Give the extent of all Plasmodium ovale-infected red blood cells.
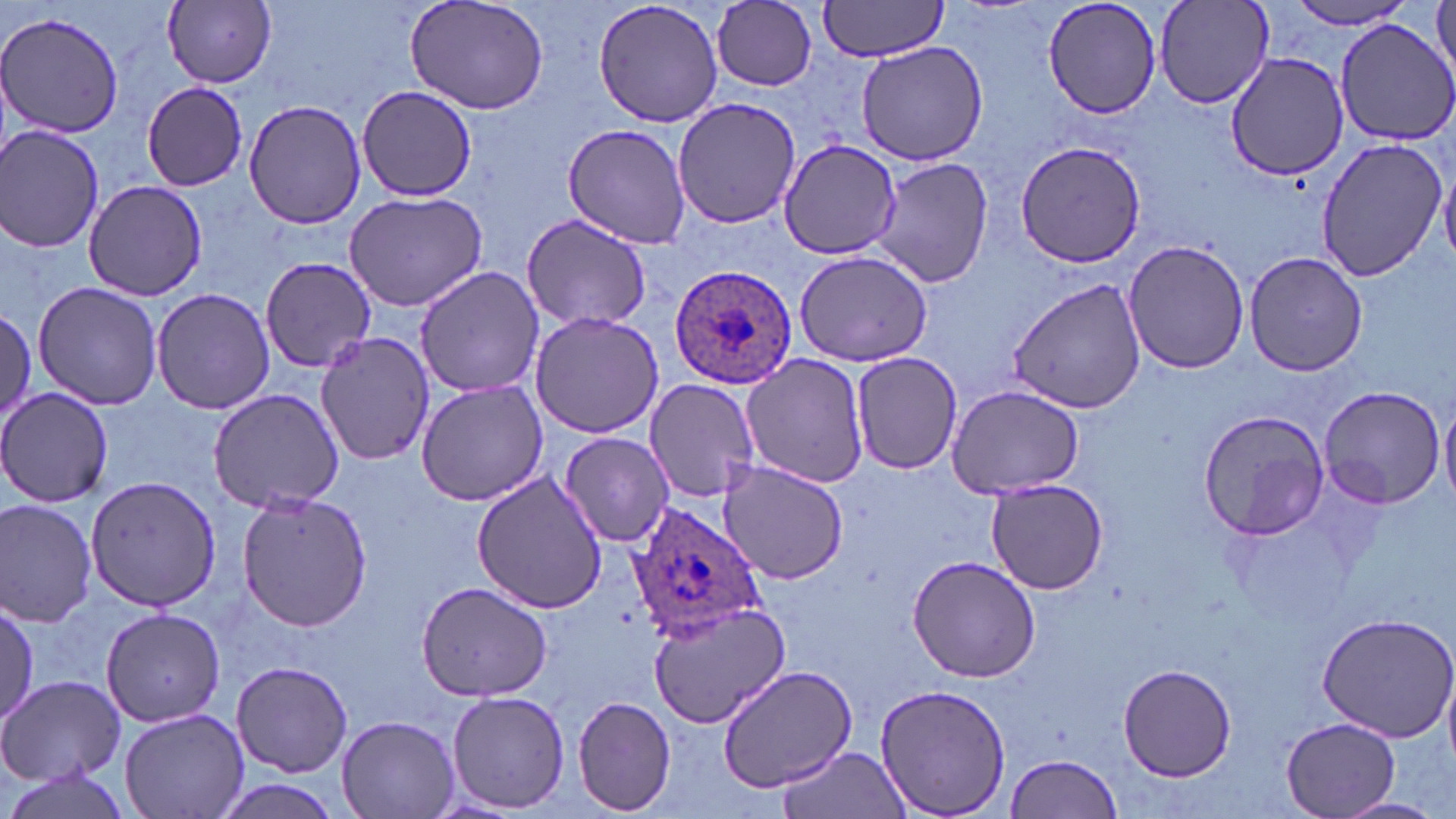

Approximate bounding boxes as named x1/y1/x2/y2 corners in pixels.
Plasmodium ovale-infected red blood cells: (x1=669, y1=262, x2=799, y2=389), (x1=626, y1=502, x2=766, y2=644).

slide-level diagnosis = Plasmodium ovale
modality = optical microscopy
image size = 1456×819 pixels
stain = May-Grünwald-Giemsa
magnification = 1000x
uninfected red blood cell locations = approximate bounding boxes as named x1/y1/x2/y2 corners in pixels: (x1=163, y1=0, x2=277, y2=88), (x1=404, y1=0, x2=552, y2=116), (x1=592, y1=0, x2=725, y2=129), (x1=817, y1=0, x2=953, y2=61), (x1=1043, y1=0, x2=1162, y2=120), (x1=1430, y1=0, x2=1456, y2=88), (x1=708, y1=1, x2=821, y2=93), (x1=1153, y1=2, x2=1274, y2=109), (x1=1282, y1=2, x2=1422, y2=30), (x1=1, y1=11, x2=125, y2=139), (x1=1332, y1=17, x2=1456, y2=147), (x1=854, y1=41, x2=990, y2=167), (x1=1224, y1=51, x2=1350, y2=182), (x1=142, y1=82, x2=249, y2=192), (x1=356, y1=85, x2=477, y2=202), (x1=672, y1=96, x2=804, y2=228), (x1=243, y1=98, x2=367, y2=230), (x1=561, y1=120, x2=694, y2=250), (x1=1, y1=125, x2=104, y2=253), (x1=1314, y1=134, x2=1447, y2=283), (x1=776, y1=138, x2=906, y2=260), (x1=1014, y1=140, x2=1145, y2=267), (x1=869, y1=156, x2=993, y2=290), (x1=1439, y1=162, x2=1456, y2=267), (x1=82, y1=179, x2=208, y2=300), (x1=343, y1=191, x2=487, y2=312), (x1=520, y1=213, x2=653, y2=334), (x1=1123, y1=239, x2=1251, y2=374), (x1=793, y1=249, x2=934, y2=368), (x1=1244, y1=250, x2=1366, y2=376), (x1=261, y1=259, x2=376, y2=374), (x1=414, y1=266, x2=547, y2=397), (x1=1007, y1=278, x2=1146, y2=413), (x1=32, y1=282, x2=164, y2=411), (x1=151, y1=286, x2=274, y2=415), (x1=0, y1=305, x2=35, y2=429), (x1=529, y1=311, x2=663, y2=439), (x1=316, y1=333, x2=437, y2=467), (x1=852, y1=352, x2=962, y2=475), (x1=741, y1=354, x2=872, y2=488), (x1=646, y1=377, x2=762, y2=501), (x1=415, y1=379, x2=550, y2=505), (x1=944, y1=385, x2=1087, y2=497), (x1=1316, y1=386, x2=1448, y2=510), (x1=1, y1=387, x2=114, y2=508), (x1=208, y1=387, x2=345, y2=514), (x1=1439, y1=396, x2=1456, y2=513), (x1=1197, y1=409, x2=1329, y2=538), (x1=559, y1=431, x2=674, y2=547), (x1=718, y1=462, x2=848, y2=584), (x1=471, y1=471, x2=608, y2=614), (x1=86, y1=476, x2=220, y2=611), (x1=984, y1=478, x2=1107, y2=596), (x1=234, y1=490, x2=373, y2=632), (x1=0, y1=498, x2=100, y2=628), (x1=906, y1=554, x2=1041, y2=683), (x1=415, y1=581, x2=551, y2=701), (x1=647, y1=600, x2=790, y2=730), (x1=1, y1=602, x2=40, y2=727), (x1=99, y1=608, x2=227, y2=728), (x1=1317, y1=612, x2=1456, y2=742), (x1=232, y1=660, x2=352, y2=777), (x1=1118, y1=663, x2=1238, y2=781), (x1=718, y1=665, x2=857, y2=791), (x1=0, y1=673, x2=124, y2=788), (x1=874, y1=682, x2=1011, y2=818), (x1=445, y1=688, x2=569, y2=813), (x1=572, y1=696, x2=677, y2=815), (x1=119, y1=707, x2=248, y2=819), (x1=337, y1=715, x2=459, y2=819), (x1=1282, y1=717, x2=1399, y2=817), (x1=775, y1=746, x2=914, y2=819), (x1=1004, y1=753, x2=1123, y2=818), (x1=0, y1=769, x2=136, y2=819), (x1=1335, y1=796, x2=1448, y2=817)
preparation = thin blood film
field of view = one of a larger specimen